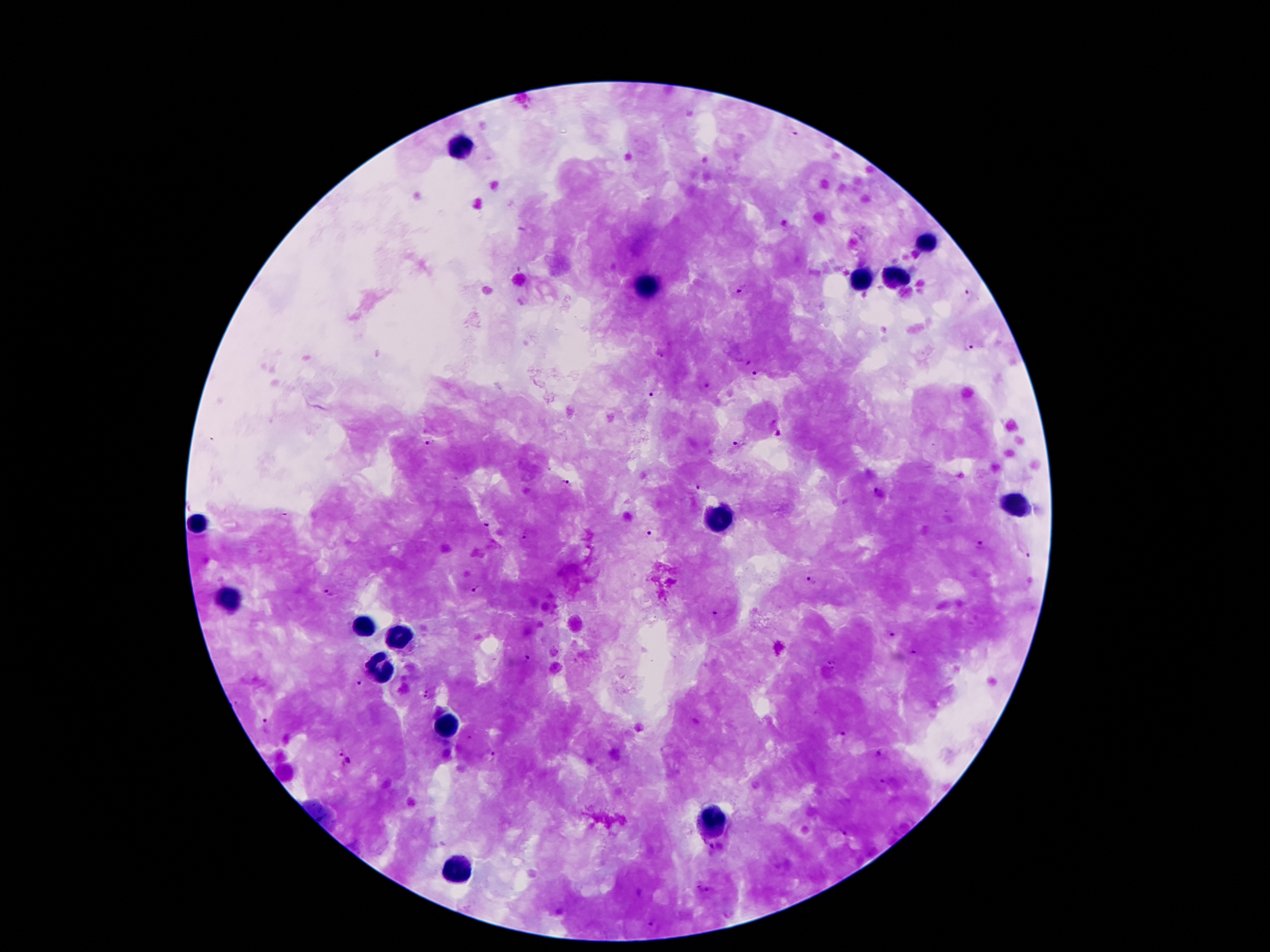 Approximate centers as {x, y} in pixels. Plasmodium parasite locations: {793, 131}, {519, 268}, {743, 288}, {968, 294}, {969, 346}, {756, 375}, {706, 384}, {651, 396}, {779, 433}, {430, 443}, {739, 444}, {567, 483}, {698, 487}, {879, 495}, {486, 527}, {651, 534}, {530, 535}, {981, 545}, {1029, 554}, {810, 582}, {475, 588}, {329, 592}, {717, 612}, {893, 634}, {912, 651}, {529, 659}, {428, 685}, {362, 686}, {426, 699}, {265, 725}, {841, 734}, {340, 752}, {491, 754}, {883, 754}, {348, 761}, {882, 785}, {716, 848}, {710, 888}, {699, 890}, {641, 894}, {560, 912}, {651, 923}. Leukocyte locations: {462, 147}, {930, 244}, {898, 279}, {863, 283}, {644, 290}, {1014, 508}, {722, 514}, {201, 521}, {235, 601}, {365, 626}, {398, 634}, {382, 664}, {447, 727}, {714, 821}, {455, 869}. Image is 1270×952 pixels. Smartphone photograph taken through the microscope eyepiece. Thick blood film. Patient malaria status: infected with Plasmodium falciparum. Single field of view. Giemsa stain. 100x magnification.